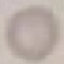

Summary:
  - Malaria status: uninfected
  - Image type: automatically extracted cell patch, resized to 64 × 64 pixels
  - Stain: Giemsa
  - Capture: smartphone through the microscope eyepiece
  - Preparation: thin blood smear